Assess this cell for malaria.
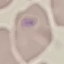
Uninfected.

Acquired by smartphone through the microscope eyepiece. Giemsa-stained preparation. Automatically extracted cell patch, resized to 64 × 64 pixels. Thin blood film.